Assess this cell for malaria.
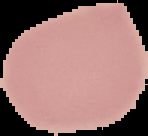

It is uninfected.

Image is 148×136 pixels. From a thin blood smear. Cell region segmented out of the field of view; the surrounding area is masked to black.